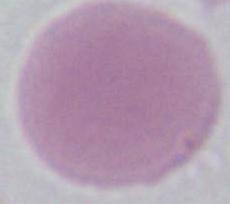
An erythrocyte is shown. Captured at 1000x magnification. Micrograph.